Report the malaria status of this cell.
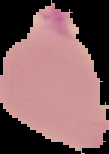

Uninfected.

{
  "image_size": "109×154 pixels",
  "image_type": "segmented cell region on a black background",
  "preparation": "thin blood film"
}